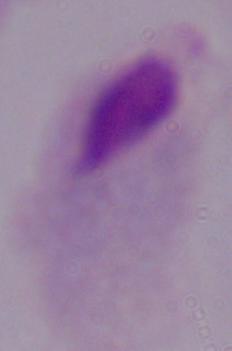
modality = photomicrograph
magnification = 1000x
identification = trichomonad